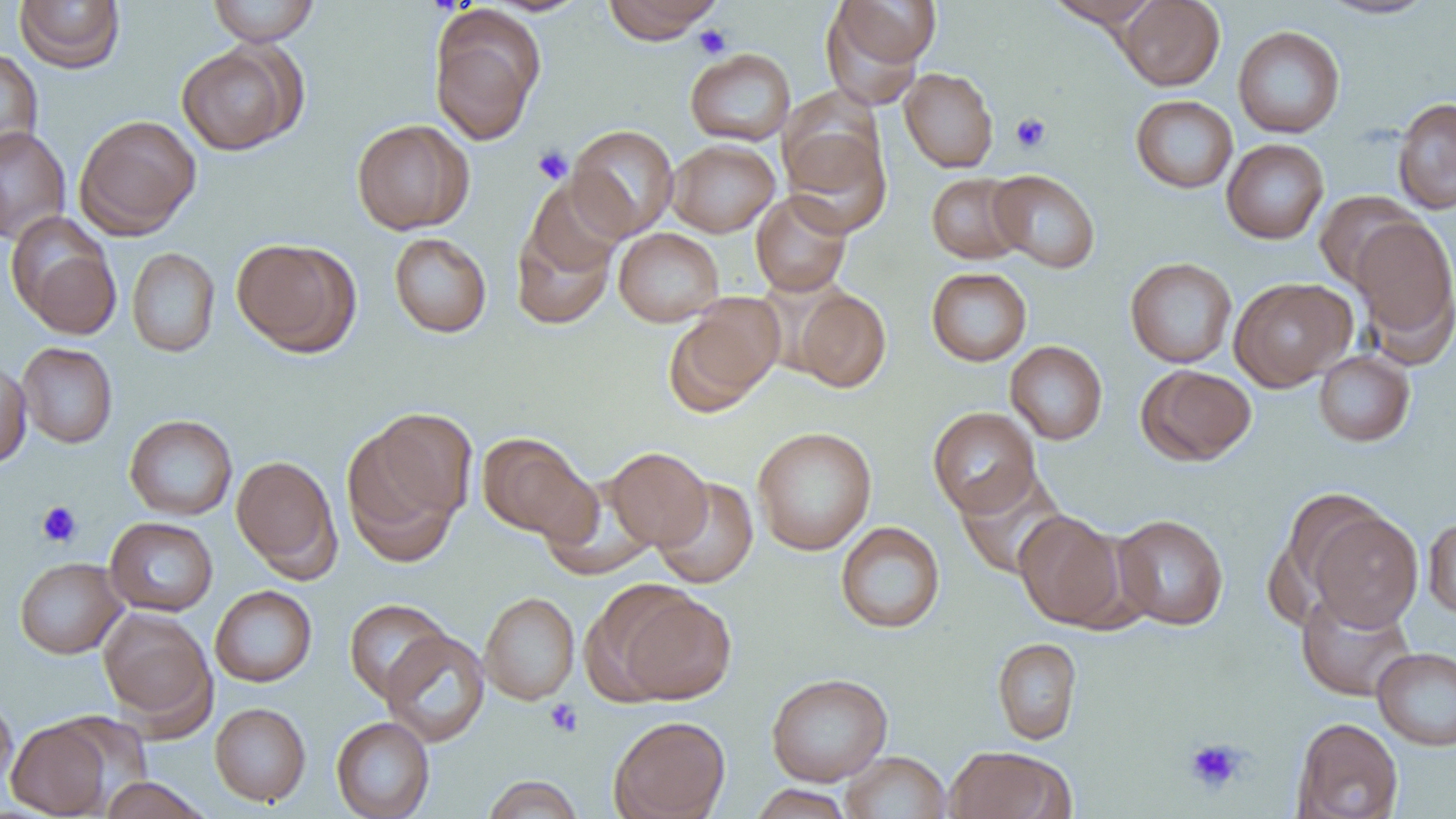
Approximate bounding boxes as (x1, y1, x2, y2) in pixels. Uninfected red blood cell locations: (207, 0, 320, 46), (483, 0, 592, 16), (602, 0, 723, 44), (822, 0, 938, 98), (1045, 0, 1161, 28), (1116, 0, 1225, 91), (1317, 0, 1437, 19), (14, 1, 126, 73), (430, 11, 543, 145), (1233, 25, 1345, 138), (176, 42, 303, 155), (0, 48, 44, 163), (685, 48, 796, 146), (899, 67, 998, 173), (1131, 95, 1238, 193), (1392, 97, 1456, 215), (74, 114, 201, 239), (351, 119, 474, 235), (567, 124, 679, 240), (781, 124, 892, 237), (0, 126, 71, 244), (1221, 138, 1329, 244), (667, 139, 780, 237), (988, 169, 1100, 273), (926, 172, 1028, 264), (522, 176, 628, 283), (750, 191, 852, 296), (1313, 191, 1422, 292), (510, 211, 618, 331), (7, 213, 122, 337), (1350, 216, 1456, 355), (613, 227, 724, 327), (389, 232, 492, 338), (231, 237, 359, 356), (127, 247, 220, 357), (1125, 257, 1237, 368), (926, 267, 1032, 366), (1229, 277, 1355, 391), (793, 288, 892, 392), (664, 297, 783, 416), (1005, 340, 1108, 444), (16, 342, 118, 448), (1313, 350, 1415, 447), (0, 359, 32, 469), (1138, 364, 1256, 466), (928, 406, 1041, 517), (124, 414, 238, 521), (341, 419, 468, 564), (752, 426, 877, 555), (477, 432, 596, 541), (605, 447, 712, 550), (230, 455, 342, 578), (955, 467, 1069, 580), (652, 477, 758, 589), (538, 479, 660, 580), (1305, 509, 1422, 631), (1014, 510, 1128, 630), (1111, 514, 1229, 630), (1423, 515, 1456, 619), (105, 516, 218, 617), (835, 521, 945, 634), (14, 557, 127, 658), (210, 585, 317, 687), (614, 588, 736, 705), (1296, 589, 1416, 702), (479, 592, 580, 705), (343, 598, 452, 702), (98, 608, 216, 731), (381, 628, 490, 747), (992, 637, 1082, 745), (1372, 646, 1456, 750), (766, 673, 893, 786), (0, 694, 17, 795), (210, 702, 311, 806), (608, 715, 730, 819), (331, 716, 435, 818), (1292, 717, 1403, 819), (6, 718, 114, 818), (945, 746, 1072, 819), (841, 751, 952, 819), (482, 775, 584, 819), (99, 776, 213, 819), (748, 784, 855, 819). Platelet locations: (693, 24, 733, 58), (1011, 112, 1051, 153), (532, 146, 573, 185), (36, 501, 82, 547), (544, 698, 583, 737), (1184, 737, 1247, 794). Slide-level diagnosis: no evidence of blood parasites. Thin blood smear. Image is 1456×819 pixels. Single field of view. Light microscopy. Captured at 1000x magnification.